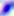
Summary:
  - Identification: Toxoplasma gondii
  - Modality: photomicrograph
  - Magnification: 400x